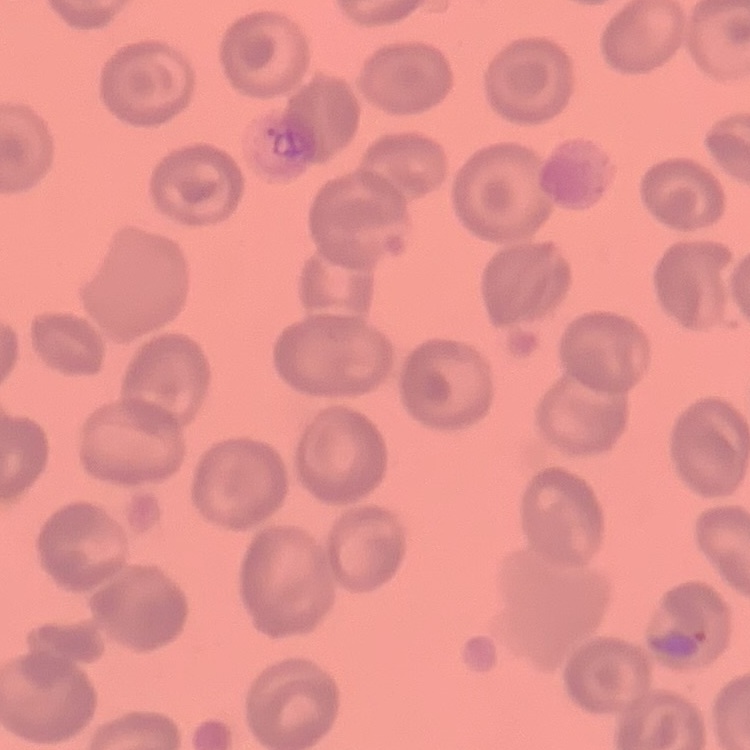

Summary:
  - Erythrocyte morphology: no rouleaux formation
  - Image type: one tile cut from a larger photomicrograph
  - Stain: Field's or Giemsa
  - Preparation: thin blood film